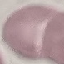
result = negative for malaria parasites
stain = Giemsa
preparation = thin blood smear
image type = cell patch, automatically extracted from a larger field of view and resized to 64 × 64 pixels
capture = smartphone camera at the microscope eyepiece